Locate Plasmodium parasites and leukocytes.
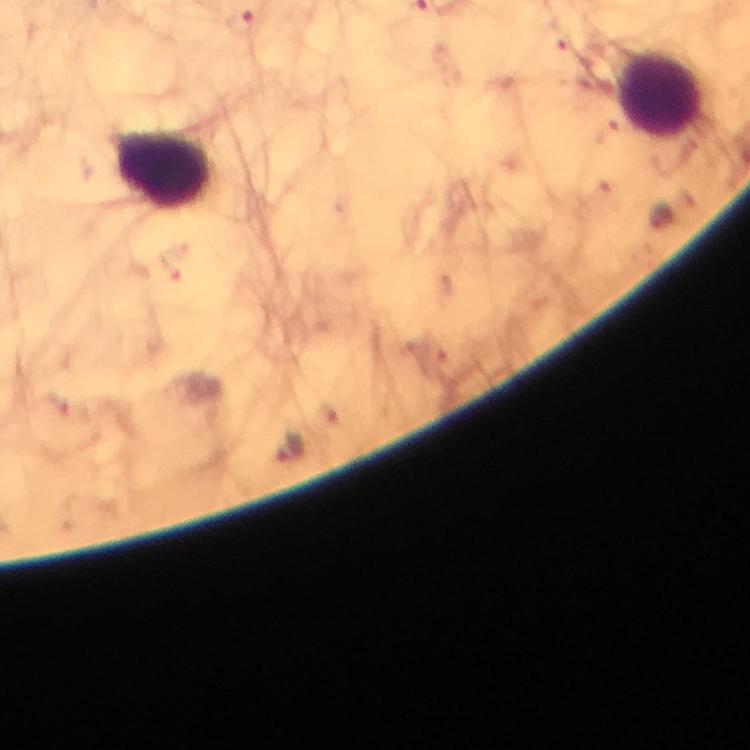

Approximate object centers, in pixels from the top-left corner.
Plasmodium parasites: (x=240, y=24), (x=561, y=36), (x=660, y=218), (x=170, y=263), (x=288, y=448).
Leukocytes: (x=659, y=94), (x=163, y=170).

{
  "magnification": "100x",
  "context": "from a malaria diagnostic workup",
  "preparation": "thick blood film",
  "image_size": "750×750 pixels",
  "immersion_oil": "used",
  "cropped_from": "a single field of view",
  "stain": "Giemsa",
  "capture": "smartphone mounted on the microscope"
}